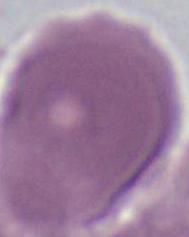
modality: photomicrograph
magnification: 1000x
identification: red blood cell